Give the extent of all Plasmodium ovale-infected red blood cells.
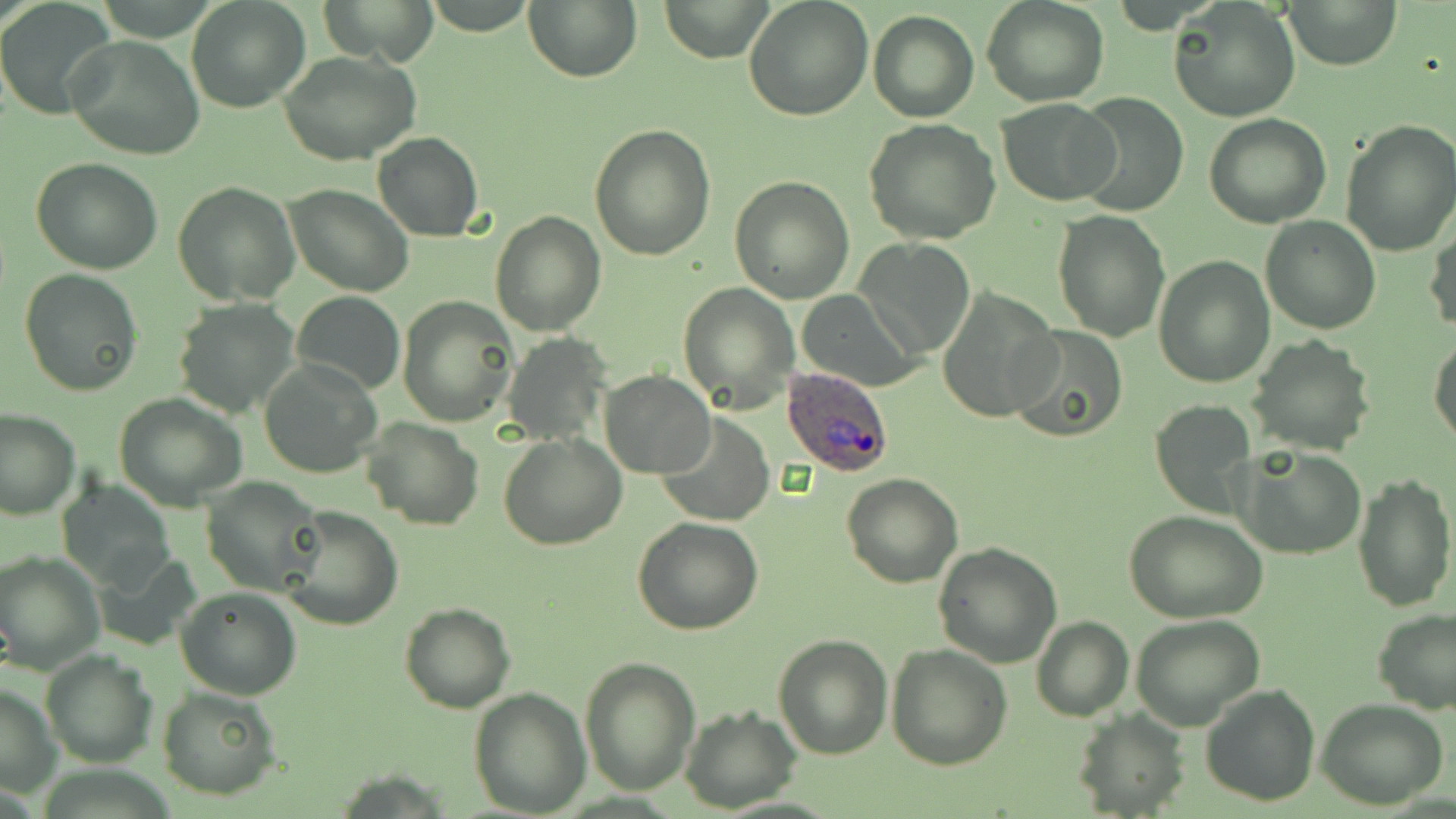

Approximate bounding boxes as (x1, y1, x2, y2) in pixels.
Plasmodium ovale-infected red blood cells: (780, 365, 896, 479).

Uninfected red blood cell locations: (186, 0, 310, 113), (321, 0, 439, 66), (524, 0, 642, 82), (660, 0, 772, 61), (743, 0, 874, 120), (981, 0, 1110, 107), (1281, 0, 1401, 71), (1168, 1, 1301, 122), (0, 5, 114, 119), (867, 11, 979, 122), (65, 36, 204, 160), (281, 51, 421, 165), (1074, 89, 1189, 217), (998, 97, 1118, 204), (1204, 112, 1331, 227), (864, 119, 1003, 243), (1340, 120, 1456, 257), (588, 124, 715, 261), (372, 132, 484, 242), (30, 157, 163, 275), (729, 175, 855, 303), (173, 180, 300, 306), (284, 184, 414, 296), (1052, 209, 1172, 341), (490, 210, 605, 335), (1260, 216, 1380, 335), (1426, 220, 1456, 337), (857, 238, 976, 357), (1153, 256, 1274, 389), (19, 269, 143, 395), (678, 282, 798, 412), (937, 289, 1061, 423), (291, 290, 405, 396), (796, 290, 922, 392), (399, 294, 519, 428), (172, 299, 302, 419), (1006, 326, 1129, 443), (503, 333, 610, 445), (1429, 334, 1456, 448), (1246, 335, 1376, 456), (260, 360, 380, 479), (600, 370, 715, 478), (114, 393, 248, 511), (1151, 399, 1258, 520), (0, 408, 80, 520), (656, 412, 775, 526), (364, 417, 486, 530), (499, 433, 626, 551), (1239, 446, 1365, 558), (1351, 470, 1456, 613), (842, 474, 964, 589), (202, 477, 327, 595), (60, 480, 177, 590), (281, 506, 403, 631), (1125, 511, 1268, 624), (632, 518, 764, 637), (933, 542, 1062, 666), (0, 550, 104, 672), (96, 551, 203, 649), (176, 586, 302, 699), (399, 603, 517, 713), (1372, 609, 1455, 714), (1131, 614, 1265, 731), (1030, 617, 1133, 722), (772, 632, 893, 758), (886, 643, 1012, 770), (42, 649, 156, 768), (580, 656, 702, 797), (0, 683, 60, 799), (1199, 683, 1323, 806), (157, 685, 282, 800), (469, 687, 593, 815), (1315, 699, 1448, 810), (680, 707, 802, 812), (1072, 708, 1189, 819). Slide-level diagnosis: Plasmodium ovale. Single field of view. Optical microscopy. May-Grünwald-Giemsa-stained preparation. Image is 1456×819 pixels. Thin blood film. Captured at 1000x magnification.